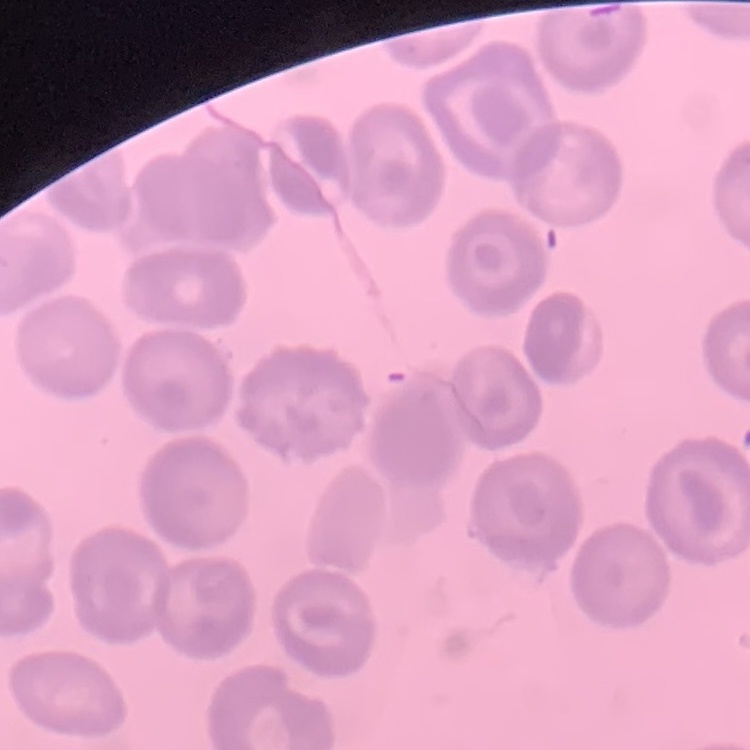

Summary:
  - Erythrocyte morphology: no rouleaux formation
  - Image type: square crop of a larger photomicrograph
  - Preparation: thin peripheral smear
  - Stain: Field's or Giemsa